Evaluate for parasitized red blood cells.
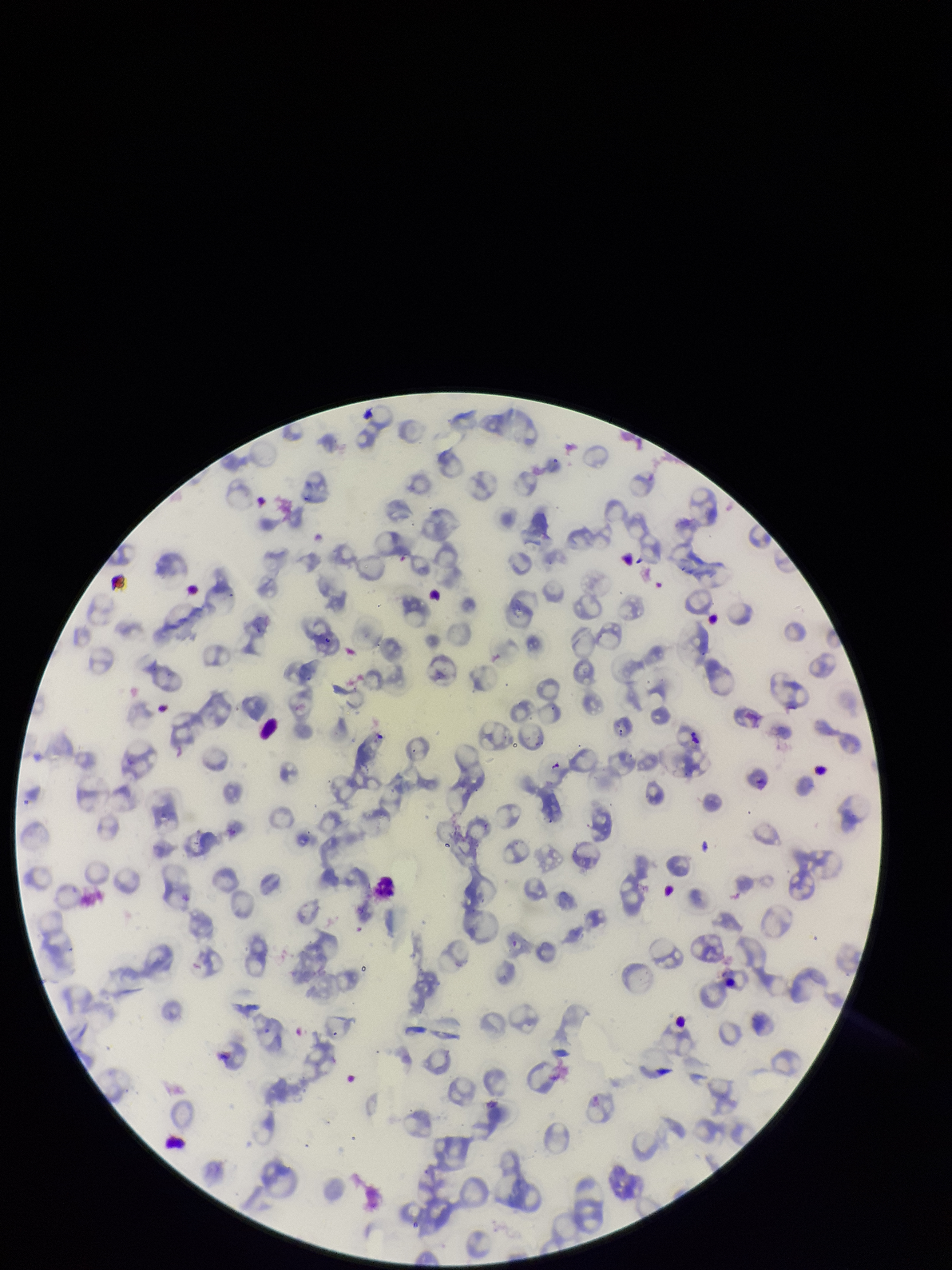

None identified.

Patient malaria status: positive. Stained with Giemsa. Species reported for this patient: Plasmodium falciparum. Parasitized red blood cell count: 0. One field from this slide. Red blood cell count: 86. Image is 952×1270 pixels. Photographed through the microscope eyepiece with a smartphone camera. Preparation: thin smear.